Comment on the background quality.
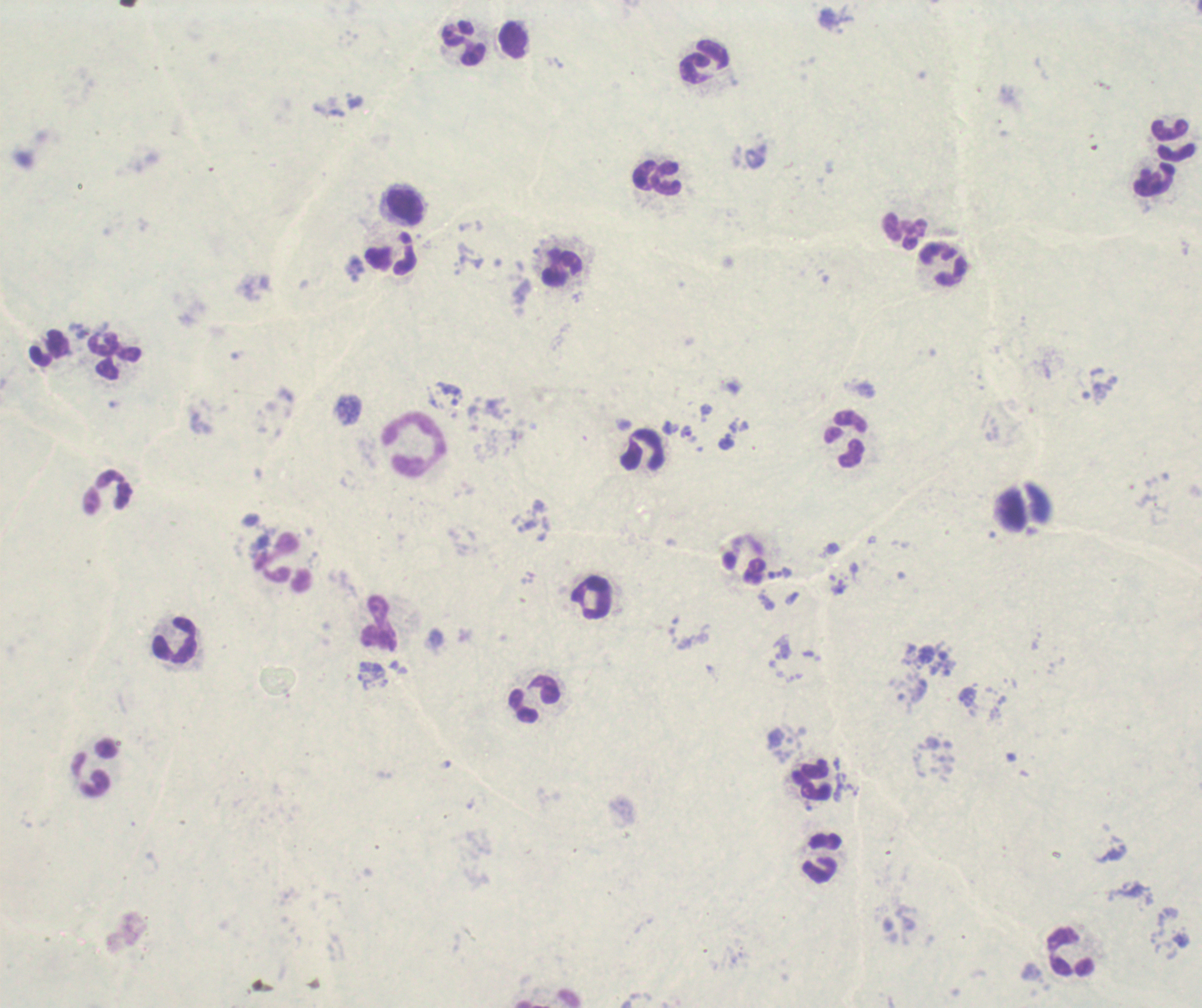

Unsatisfactory.

{
  "context": "previously used in a real diagnosis",
  "image_size": "1202×1008 pixels",
  "magnification": "100x",
  "leukocyte_locations": "approximate object centers, in pixels from the top-left corner: (x=514, y=41), (x=464, y=44), (x=705, y=62), (x=1170, y=131), (x=1175, y=153), (x=645, y=175), (x=667, y=178), (x=1154, y=179), (x=406, y=206), (x=906, y=231), (x=391, y=260), (x=943, y=264), (x=562, y=267), (x=114, y=356), (x=846, y=440), (x=414, y=443), (x=643, y=449), (x=107, y=492), (x=287, y=563), (x=589, y=599), (x=379, y=622), (x=174, y=641), (x=534, y=699), (x=95, y=768), (x=812, y=779), (x=822, y=858), (x=1071, y=954)",
  "stain": "Romanowsky",
  "result": "positive for malaria parasites",
  "field_of_view": "single",
  "trophozoite_locations": "approximate object centers, in pixels from the top-left corner: (x=450, y=393), (x=685, y=433), (x=838, y=586)",
  "preparation": "thick smear of blood"
}